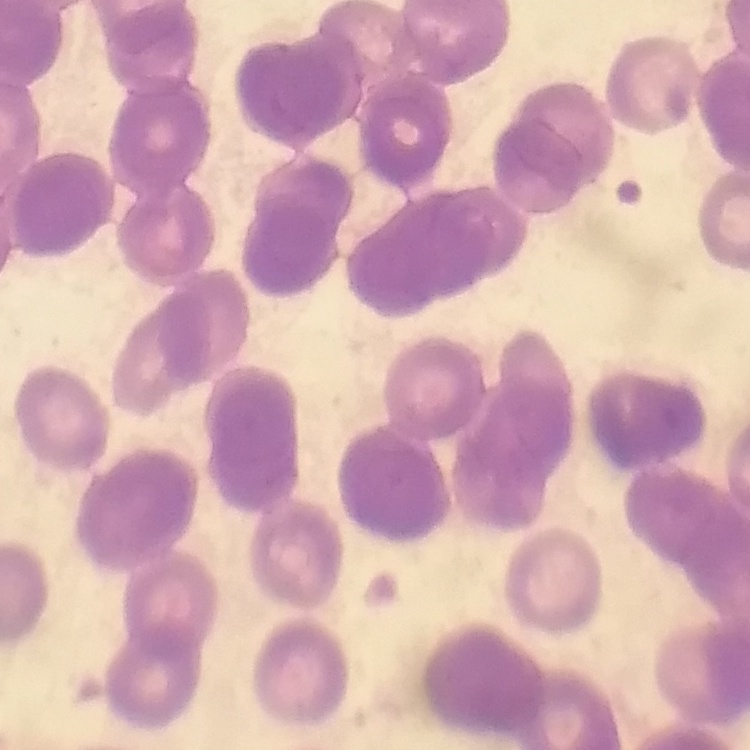
The red blood cells show rouleaux formation. Stained with either Field's or Giemsa. Thin blood film. Square crop of a larger photomicrograph.